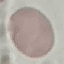

result = negative for malaria parasites
image type = automatically extracted cell patch, resized to 64 × 64 pixels
capture = smartphone through the microscope eyepiece
preparation = thin blood film
stain = Giemsa